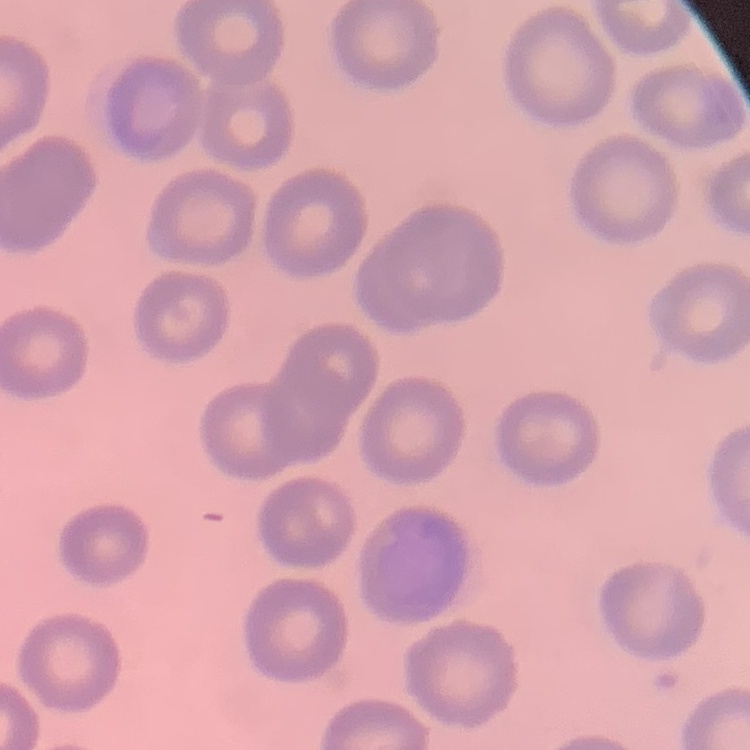
Summary:
  - Erythrocyte morphology: no rouleaux formation
  - Preparation: thin peripheral smear
  - Stain: Field's or Giemsa
  - Image type: square crop of a larger photomicrograph